Name the blood parasite species.
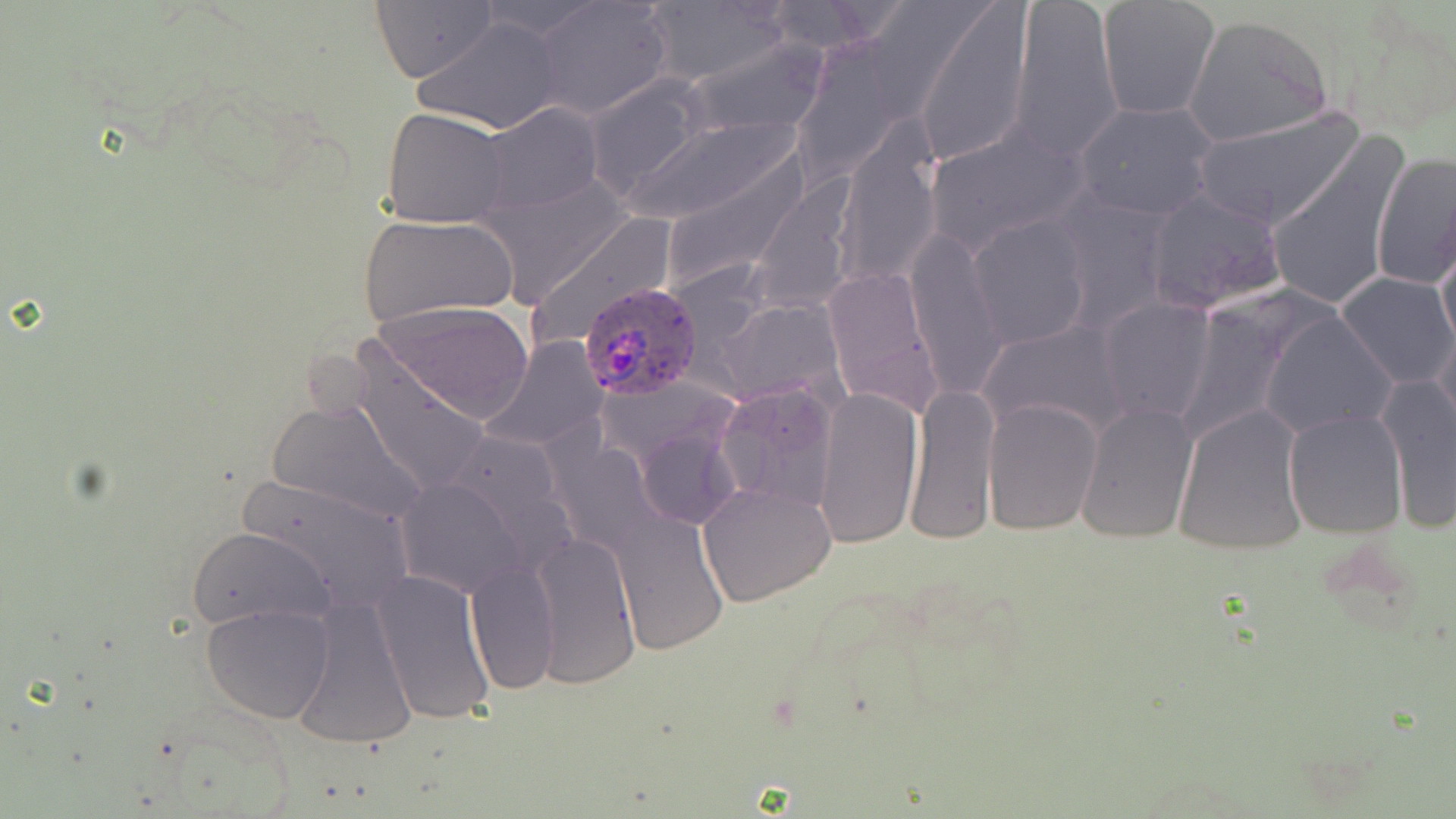
Plasmodium ovale.

magnification = 1000x
Plasmodium ovale-infected red blood cell locations = approximate bounding boxes as named x1/y1/x2/y2 corners in pixels: (x1=579, y1=281, x2=705, y2=403)
modality = optical microscopy
field of view = one of a larger specimen
stain = May-Grünwald-Giemsa
uninfected red blood cell locations = approximate bounding boxes as named x1/y1/x2/y2 corners in pixels: (x1=758, y1=0, x2=896, y2=56), (x1=1010, y1=0, x2=1122, y2=162), (x1=1096, y1=0, x2=1220, y2=121), (x1=370, y1=1, x2=498, y2=84), (x1=532, y1=1, x2=673, y2=119), (x1=913, y1=2, x2=1034, y2=168), (x1=645, y1=3, x2=791, y2=87), (x1=1334, y1=5, x2=1456, y2=139), (x1=1182, y1=14, x2=1333, y2=147), (x1=414, y1=16, x2=566, y2=134), (x1=682, y1=35, x2=830, y2=142), (x1=583, y1=75, x2=710, y2=198), (x1=1072, y1=98, x2=1220, y2=221), (x1=478, y1=103, x2=603, y2=215), (x1=382, y1=106, x2=513, y2=228), (x1=1191, y1=107, x2=1363, y2=232), (x1=617, y1=111, x2=803, y2=230), (x1=834, y1=123, x2=943, y2=287), (x1=925, y1=124, x2=1091, y2=260), (x1=1265, y1=133, x2=1409, y2=315), (x1=655, y1=149, x2=814, y2=296), (x1=1370, y1=149, x2=1456, y2=292), (x1=1140, y1=190, x2=1290, y2=319), (x1=359, y1=213, x2=520, y2=327), (x1=969, y1=215, x2=1093, y2=352), (x1=1436, y1=225, x2=1456, y2=359), (x1=905, y1=232, x2=1008, y2=398), (x1=821, y1=266, x2=942, y2=416), (x1=1337, y1=272, x2=1456, y2=390), (x1=1098, y1=297, x2=1216, y2=427), (x1=373, y1=299, x2=534, y2=424), (x1=1260, y1=308, x2=1398, y2=438), (x1=977, y1=319, x2=1133, y2=443), (x1=483, y1=337, x2=606, y2=452), (x1=347, y1=345, x2=493, y2=499), (x1=1377, y1=372, x2=1456, y2=532), (x1=906, y1=380, x2=1000, y2=546), (x1=715, y1=383, x2=839, y2=514), (x1=811, y1=386, x2=924, y2=550), (x1=265, y1=397, x2=428, y2=528), (x1=983, y1=399, x2=1103, y2=535), (x1=1075, y1=401, x2=1199, y2=544), (x1=1172, y1=403, x2=1308, y2=555), (x1=1282, y1=408, x2=1407, y2=540), (x1=389, y1=468, x2=541, y2=601), (x1=231, y1=473, x2=417, y2=616), (x1=698, y1=483, x2=837, y2=607), (x1=611, y1=512, x2=728, y2=654), (x1=186, y1=526, x2=336, y2=633), (x1=531, y1=529, x2=642, y2=692), (x1=465, y1=561, x2=559, y2=696), (x1=370, y1=567, x2=497, y2=729), (x1=291, y1=597, x2=417, y2=751), (x1=201, y1=603, x2=334, y2=724)
preparation = thin blood smear
image size = 1456×819 pixels